Classify the preparation.
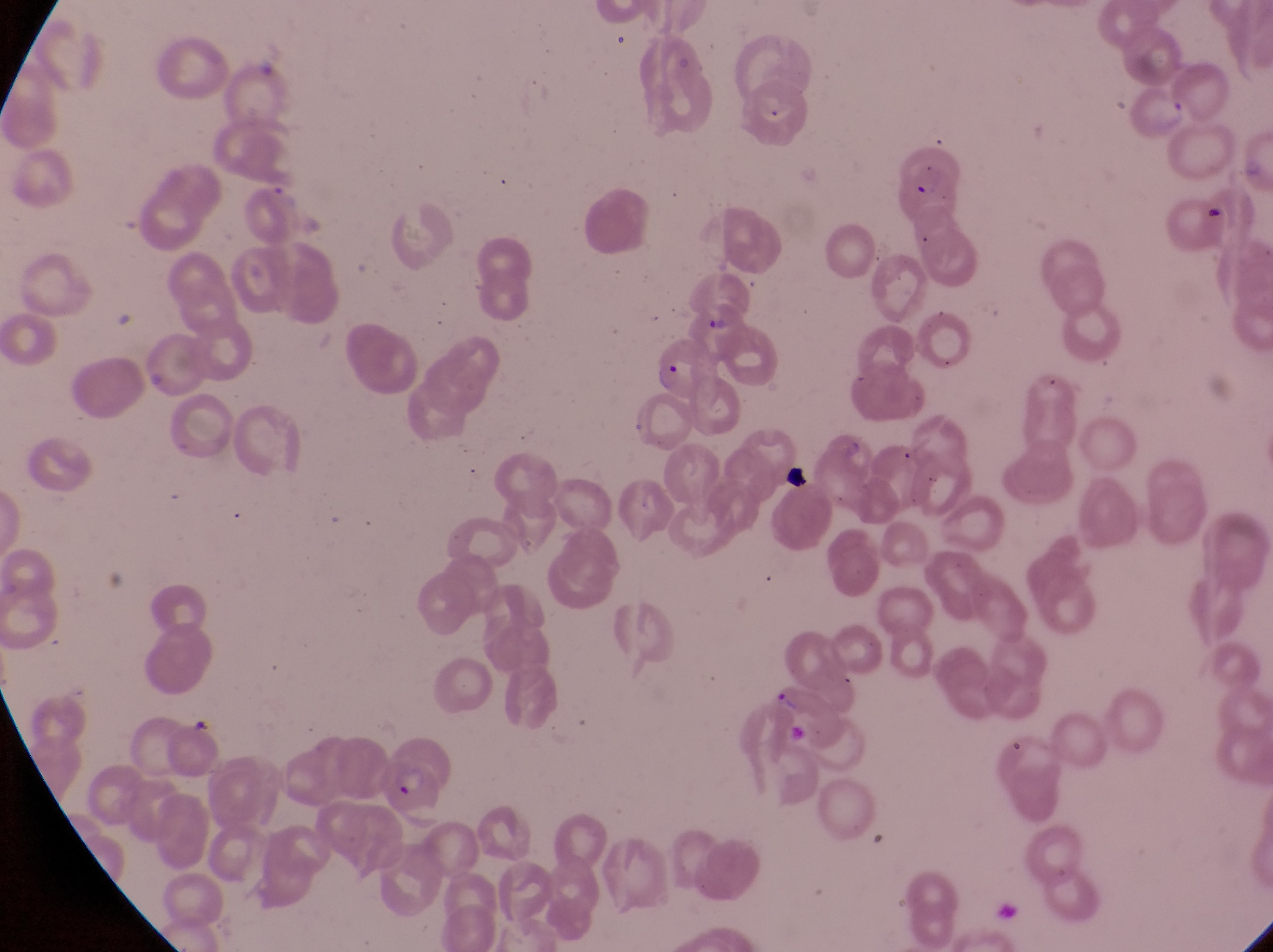
Thin blood film.

Approximate bounding boxes as {left, top, right, bottom} in pixels.
Summary:
  - Parasitised red blood cell locations: {891, 142, 961, 219}, {240, 184, 305, 242}, {654, 340, 726, 405}, {764, 679, 852, 746}, {365, 752, 452, 822}
  - Artifact (platelet-like body, stain precipitate, or debris) locations: {1199, 197, 1238, 230}, {776, 455, 821, 505}
  - Capture: smartphone photograph through the eyepiece of an Olympus CX-23 microscope
  - Image size: 1273×952 pixels
  - Magnification: 1000x
  - Country: Uganda
  - Field of view: single